State the preparation type.
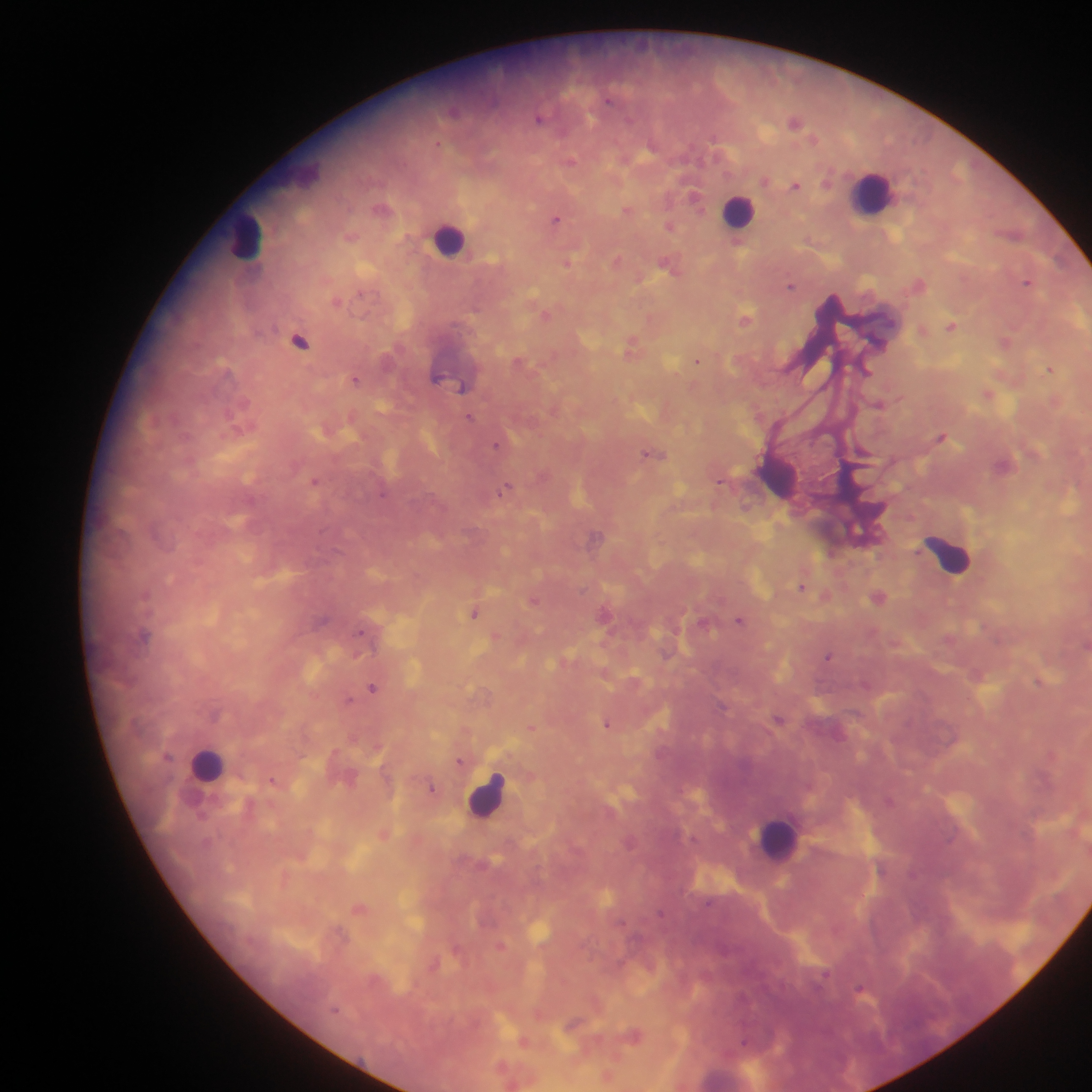

Thick blood film.

image size = 1092×1092 pixels
capture = mobile-phone photograph through a microscope
field of view = single
leukocyte locations = approximate centers as (x, y) in pixels: (871, 192), (739, 210), (246, 236), (449, 240), (777, 477), (948, 555), (208, 764), (487, 796), (777, 839), (726, 1075)
Plasmodium parasite locations = approximate centers as (x, y) in pixels: (453, 111), (540, 118), (795, 121), (438, 143), (571, 161), (796, 185), (696, 197), (383, 209), (627, 209), (555, 219), (669, 225), (351, 235), (618, 259), (568, 262), (670, 265), (1028, 281), (919, 283), (790, 286), (337, 300), (545, 313), (651, 317), (746, 319), (952, 326), (923, 329), (300, 340), (1006, 341), (633, 346), (697, 360), (520, 362), (1050, 369), (438, 377), (355, 378), (462, 386), (988, 393), (878, 403), (470, 416), (244, 426), (942, 435), (498, 445), (653, 454), (1004, 465), (316, 481), (720, 481), (507, 488), (745, 507), (596, 537), (802, 586), (827, 595), (878, 597), (534, 599), (475, 613), (605, 613), (740, 620), (705, 623), (144, 635), (496, 636), (1085, 644), (828, 657), (1041, 681), (373, 688), (349, 700), (779, 718), (608, 724), (532, 726), (1052, 753), (461, 760), (273, 780), (432, 787), (385, 832), (359, 909), (501, 945), (861, 989), (575, 1023), (633, 1035), (524, 1041), (609, 1076)
country = Ghana